Report the malaria status of this cell.
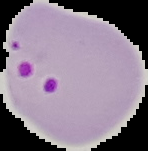

It is parasitized.

Summary:
  - Image type: segmented cell region on a black background
  - Preparation: thin blood smear
  - Image size: 148×151 pixels